Assess this cell for malaria.
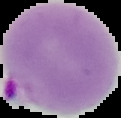
Parasitized.

Summary:
  - Image size: 121×118 pixels
  - Preparation: thin blood smear
  - Image type: cell region segmented out of the field of view; surrounding area masked to black